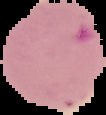

{
  "preparation": "thin blood smear",
  "image_size": "106×115 pixels",
  "malaria_status": "parasitized",
  "image_type": "segmented cell region with the area outside set to black"
}